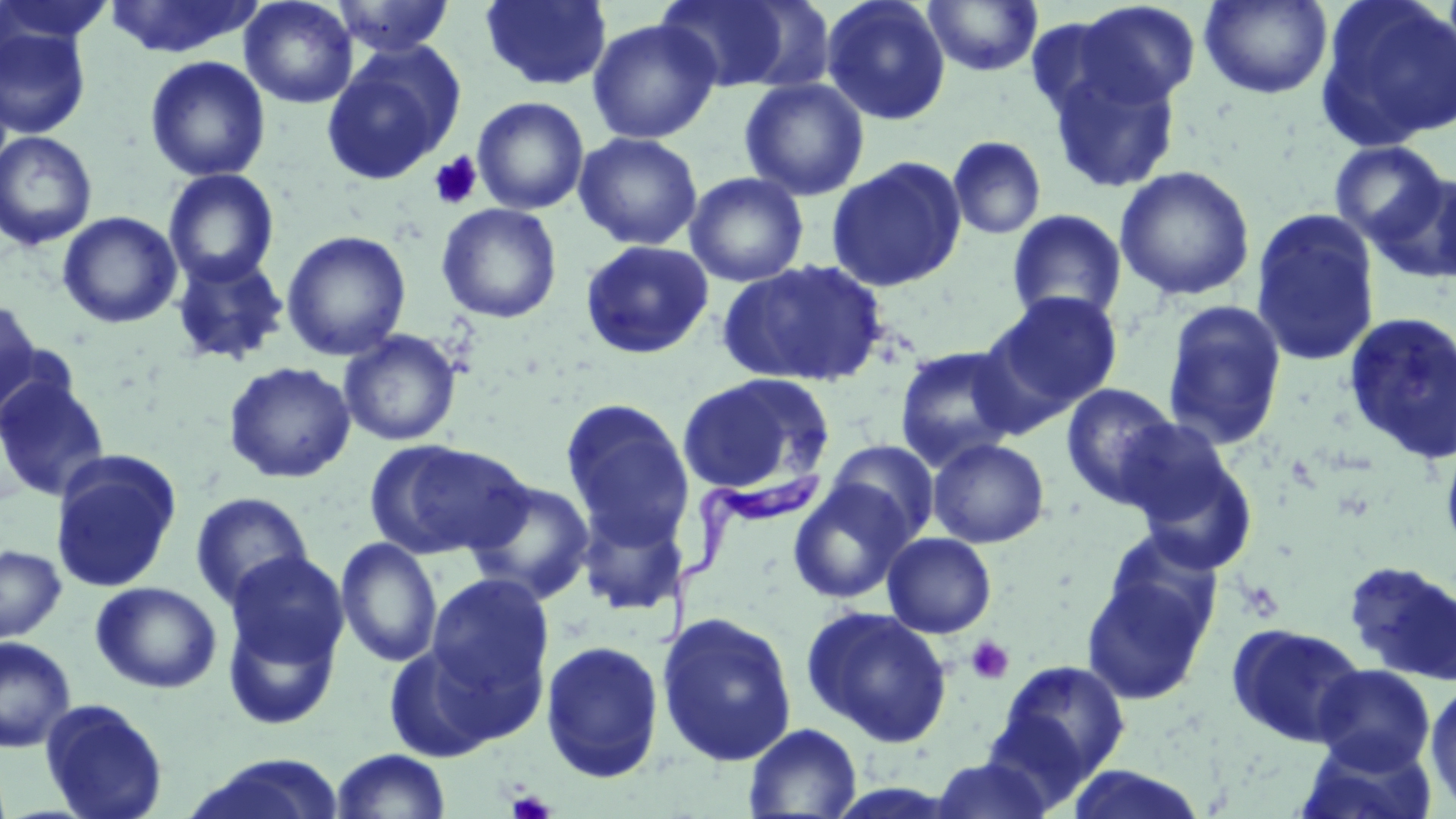

{
  "slide_level_diagnosis": "Trypanosoma brucei",
  "image_size": "1456×819 pixels",
  "modality": "light microscopy",
  "trypanosoma_brucei_locations": "approximate bounding boxes as (x1,y1)-(x2,y2) corner pairs in pixels: (659,465)-(826,651)",
  "preparation": "thin blood film",
  "uninfected_red_blood_cell_locations": "approximate bounding boxes as (x1,y1)-(x2,y2) corner pairs in pixels: (0,0)-(114,51), (104,0)-(262,59), (239,0)-(358,109), (331,0)-(456,58), (480,0)-(612,91), (821,0)-(951,126), (1199,0)-(1332,100), (1315,0)-(1456,151), (655,1)-(815,94), (924,1)-(1043,76), (1063,1)-(1203,114), (587,18)-(721,144), (0,26)-(92,139), (321,43)-(466,186), (145,55)-(270,182), (1043,56)-(1184,194), (739,78)-(869,200), (472,97)-(589,215), (0,131)-(99,251), (574,132)-(703,250), (947,136)-(1046,240), (1329,140)-(1450,247), (827,157)-(967,292), (1114,165)-(1256,302), (163,169)-(280,287), (685,172)-(809,287), (1374,174)-(1456,284), (1429,174)-(1456,291), (436,203)-(562,324), (1250,208)-(1382,368), (1006,209)-(1128,325), (58,211)-(182,329), (281,230)-(412,361), (580,240)-(714,360), (170,252)-(290,366), (718,258)-(890,389), (985,291)-(1124,418), (0,297)-(43,419), (1161,300)-(1287,451), (1343,311)-(1456,465), (339,329)-(462,447), (894,345)-(1023,471), (223,361)-(357,484), (0,373)-(111,503), (677,373)-(834,497), (1060,383)-(1180,508), (560,399)-(695,547), (1440,433)-(1456,563), (1123,436)-(1259,574), (927,438)-(1050,548), (365,439)-(529,560), (827,440)-(939,542), (49,452)-(182,594), (464,477)-(596,605), (788,480)-(914,604), (190,492)-(314,609), (576,499)-(688,616), (882,532)-(997,638), (335,537)-(443,668), (0,544)-(67,643), (224,551)-(349,677), (1344,560)-(1456,685), (1081,561)-(1217,706), (424,573)-(556,726), (90,581)-(222,694), (221,602)-(343,731), (801,606)-(953,747), (656,611)-(798,767), (1227,622)-(1367,747), (0,636)-(76,752), (381,639)-(509,761), (539,639)-(666,783), (991,659)-(1131,792), (1312,663)-(1436,774), (1425,680)-(1456,814), (39,698)-(169,819), (743,723)-(862,817), (1296,735)-(1438,819), (329,749)-(452,819), (184,754)-(347,819), (929,757)-(1056,819), (1062,765)-(1210,819)",
  "field_of_view": "one of a larger specimen",
  "stain": "May-Grünwald-Giemsa",
  "magnification": "1000x",
  "platelet_locations": "approximate bounding boxes as (x1,y1)-(x2,y2) corner pairs in pixels: (428,152)-(483,209), (966,636)-(1015,685), (507,790)-(555,819)"
}